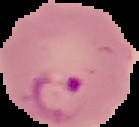
Cell region segmented out of the field of view; the surrounding area is masked to black. From a thin blood film. Result: malaria parasites identified. Image is 139×127 pixels.